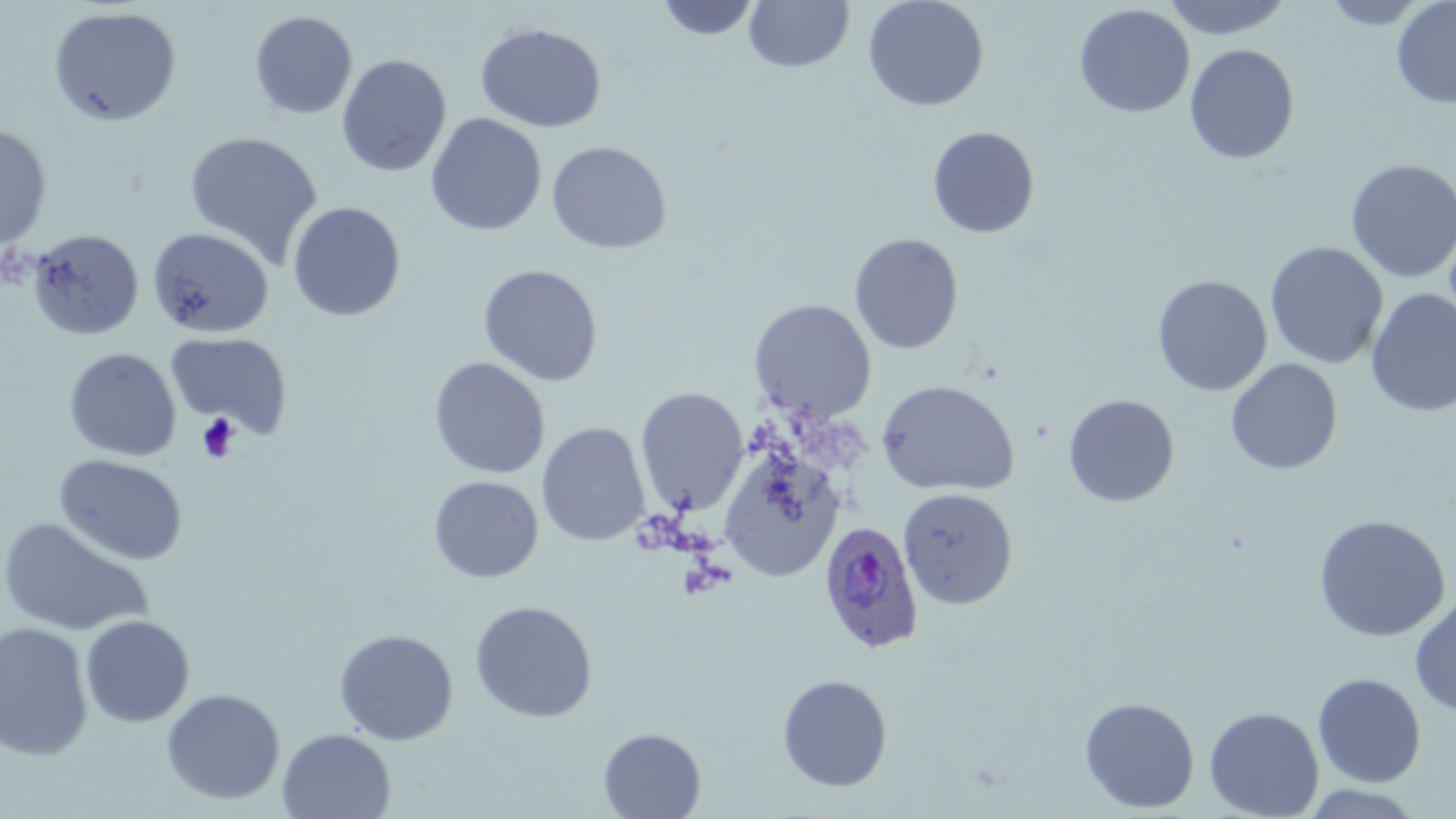
Summary:
  - Coordinate format: approximate bounding boxes as [x1, y1, x2, y2] in pixels
  - Uninfected red blood cell locations: [655, 0, 762, 41], [862, 0, 989, 112], [1161, 0, 1293, 41], [1320, 0, 1432, 30], [1391, 0, 1456, 110], [744, 1, 855, 73], [1073, 4, 1195, 118], [47, 6, 182, 128], [249, 11, 358, 121], [475, 22, 607, 134], [1184, 43, 1300, 165], [335, 54, 452, 178], [425, 113, 547, 237], [0, 124, 52, 251], [927, 125, 1040, 239], [183, 130, 324, 269], [546, 141, 672, 255], [1345, 158, 1456, 284], [286, 201, 406, 323], [146, 226, 275, 339], [26, 228, 144, 341], [848, 232, 964, 355], [1265, 242, 1388, 369], [478, 263, 603, 387], [1152, 275, 1272, 397], [1365, 289, 1456, 418], [749, 298, 877, 422], [165, 332, 293, 437], [62, 347, 182, 462], [428, 357, 550, 480], [1225, 358, 1343, 475], [876, 380, 1019, 497], [634, 387, 749, 516], [1062, 394, 1180, 507], [536, 422, 650, 547], [718, 446, 845, 584], [54, 454, 188, 566], [428, 476, 543, 583], [898, 487, 1018, 610], [1313, 514, 1451, 642], [0, 516, 153, 637], [1410, 592, 1456, 718], [469, 601, 598, 723], [80, 615, 195, 727], [0, 622, 94, 760], [333, 628, 459, 745], [1313, 673, 1427, 787], [776, 674, 893, 792], [161, 688, 285, 805], [1079, 697, 1200, 813], [1204, 706, 1324, 819], [598, 727, 706, 818], [277, 728, 396, 818], [1298, 784, 1428, 819]
  - Platelet locations: [196, 412, 241, 463]
  - Plasmodium ovale-infected red blood cell locations: [818, 519, 924, 655]
  - Slide-level diagnosis: Plasmodium ovale
  - Preparation: thin blood film
  - Magnification: 1000x
  - Field of view: single
  - Stain: May-Grünwald-Giemsa
  - Modality: optical microscopy
  - Image size: 1456×819 pixels